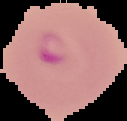

Summary:
  - Preparation: thin blood film
  - Image size: 127×121 pixels
  - Image type: segmented cell region on a black background
  - Malaria status: parasitized